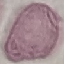

result = no malaria parasites seen
capture = smartphone through the microscope eyepiece
stain = Giemsa
preparation = thin blood smear
image type = automatically extracted cell patch, resized to 64 × 64 pixels